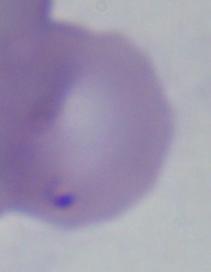 Micrograph. A Babesia parasite is seen. 1000x magnification.